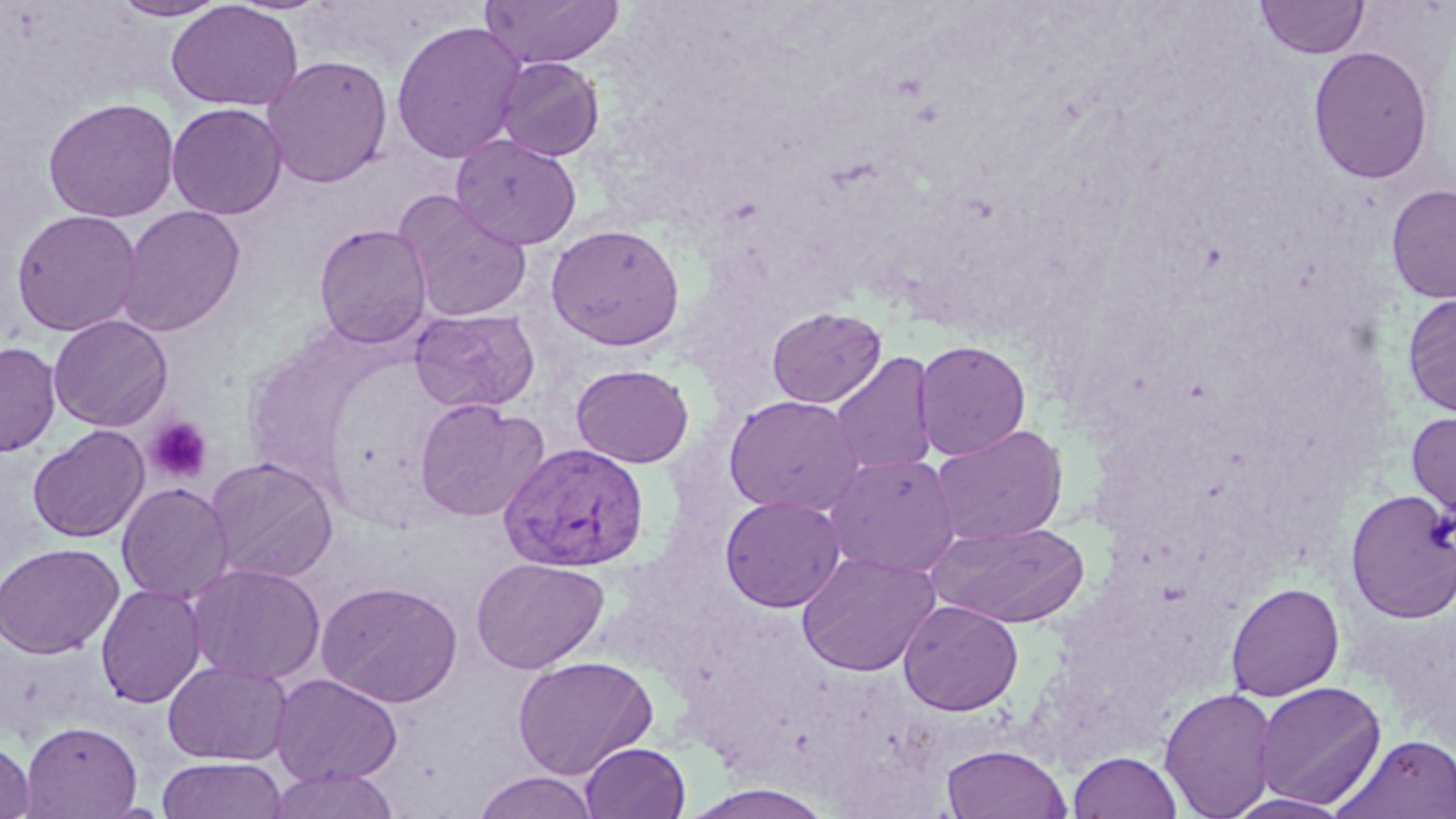
Approximate bounding boxes as (x1,y1)-(x2,y2) corner pairs in pixels. Plasmodium vivax-infected red blood cell locations: (499,442)-(651,572). Platelet locations: (145,416)-(213,484). Uninfected red blood cell locations: (479,0)-(624,69), (1255,0)-(1371,60), (110,1)-(228,21), (165,1)-(303,111), (391,20)-(527,165), (1308,46)-(1434,184), (261,55)-(393,188), (494,57)-(605,162), (43,97)-(180,223), (166,103)-(287,220), (451,134)-(582,249), (1386,183)-(1455,304), (394,190)-(533,322), (117,205)-(246,337), (11,209)-(142,337), (314,223)-(433,349), (545,224)-(685,351), (1402,293)-(1456,417), (409,307)-(540,414), (767,307)-(887,408), (49,315)-(173,432), (913,340)-(1031,461), (0,341)-(61,457), (829,351)-(938,476), (571,364)-(694,468), (723,395)-(866,517), (413,398)-(548,522), (1406,410)-(1456,522), (27,424)-(150,543), (930,424)-(1068,546), (825,452)-(960,577), (205,456)-(339,584), (117,483)-(235,605), (1347,488)-(1456,624), (720,495)-(846,612), (926,520)-(1091,628), (0,543)-(123,659), (796,551)-(941,676), (471,557)-(609,673), (188,563)-(326,685), (317,580)-(463,708), (1226,581)-(1345,701), (96,584)-(207,709), (898,599)-(1023,716), (512,656)-(659,780), (163,660)-(292,765), (270,673)-(403,787), (1253,681)-(1387,810), (1159,687)-(1278,818), (21,720)-(142,818), (1333,734)-(1456,819), (0,738)-(35,818), (580,742)-(691,819), (941,743)-(1071,819), (1068,751)-(1182,819), (157,758)-(287,818), (266,767)-(401,819), (471,771)-(601,818), (682,784)-(839,819), (1223,793)-(1355,818). Slide-level diagnosis: Plasmodium vivax. Thin blood film. May-Grünwald-Giemsa stain. Image is 1456×819 pixels. One field of a larger specimen. 1000x magnification. Light microscopy.